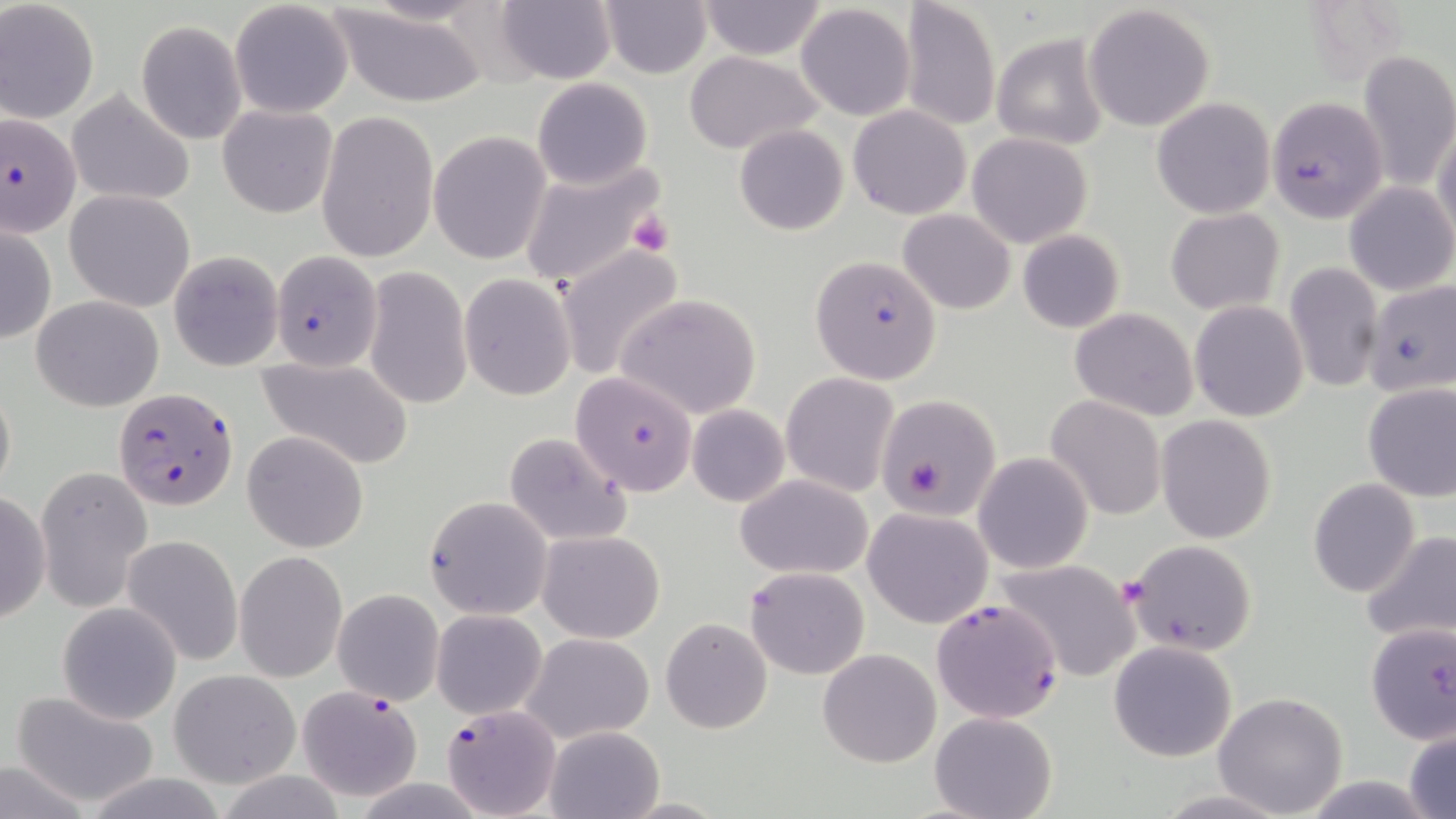
{
  "slide_level_diagnosis": "Plasmodium falciparum",
  "magnification": "1000x",
  "preparation": "thin blood film",
  "uninfected_red_blood_cell_locations": "approximate bounding boxes as (x1,y1)-(x2,y2) corner pairs in pixels: (494,0)-(617,85), (598,0)-(713,78), (901,0)-(1001,131), (0,1)-(100,123), (697,1)-(828,60), (229,2)-(354,118), (795,3)-(917,122), (323,4)-(492,108), (1083,4)-(1216,132), (136,21)-(246,144), (992,33)-(1108,149), (1358,48)-(1456,195), (683,50)-(824,154), (530,77)-(653,190), (67,88)-(196,205), (1152,97)-(1275,218), (849,104)-(972,219), (217,105)-(338,218), (315,110)-(438,264), (1433,118)-(1456,249), (733,124)-(849,235), (429,131)-(551,265), (967,131)-(1093,248), (515,158)-(664,294), (1343,180)-(1455,296), (65,188)-(196,312), (1166,208)-(1284,314), (898,209)-(1016,313), (1,220)-(56,348), (1018,230)-(1125,333), (555,244)-(688,382), (168,250)-(284,371), (1285,261)-(1384,393), (363,267)-(472,409), (459,273)-(578,400), (614,294)-(763,420), (31,295)-(164,411), (1189,300)-(1309,421), (1069,307)-(1200,421), (257,355)-(414,469), (571,370)-(698,494), (780,371)-(900,496), (0,377)-(16,502), (1361,384)-(1456,501), (874,394)-(1001,520), (1045,395)-(1166,521), (687,403)-(788,507), (1156,416)-(1276,543), (244,430)-(367,552), (503,432)-(633,546), (974,453)-(1093,573), (37,466)-(153,612), (735,473)-(875,579), (1308,477)-(1421,597), (0,489)-(50,629), (425,496)-(553,619), (864,507)-(993,628), (538,529)-(664,643), (1360,530)-(1456,646), (122,535)-(242,667), (1125,539)-(1258,657), (234,549)-(347,684), (994,558)-(1142,683), (746,566)-(869,679), (333,588)-(445,706), (57,602)-(182,725), (431,610)-(546,718), (661,618)-(772,733), (1364,621)-(1456,745), (522,632)-(656,744), (1108,640)-(1239,762), (817,648)-(941,768), (170,669)-(300,787), (8,687)-(161,807), (1212,690)-(1348,816), (930,710)-(1057,819), (1404,726)-(1456,819), (544,727)-(663,818), (0,756)-(93,819), (1296,776)-(1442,817)",
  "plasmodium_falciparum_infected_red_blood_cell_locations": "approximate bounding boxes as (x1,y1)-(x2,y2) corner pairs in pixels: (1267,96)-(1386,224), (1,112)-(82,238), (268,250)-(383,371), (810,255)-(942,384), (1369,284)-(1456,390), (112,388)-(238,511), (932,595)-(1063,723), (296,684)-(426,803), (442,703)-(561,818)",
  "modality": "optical microscopy",
  "stain": "May-Grünwald-Giemsa",
  "image_size": "1456×819 pixels",
  "field_of_view": "one of a larger specimen",
  "platelet_locations": "approximate bounding boxes as (x1,y1)-(x2,y2) corner pairs in pixels: (627,211)-(673,256)"
}